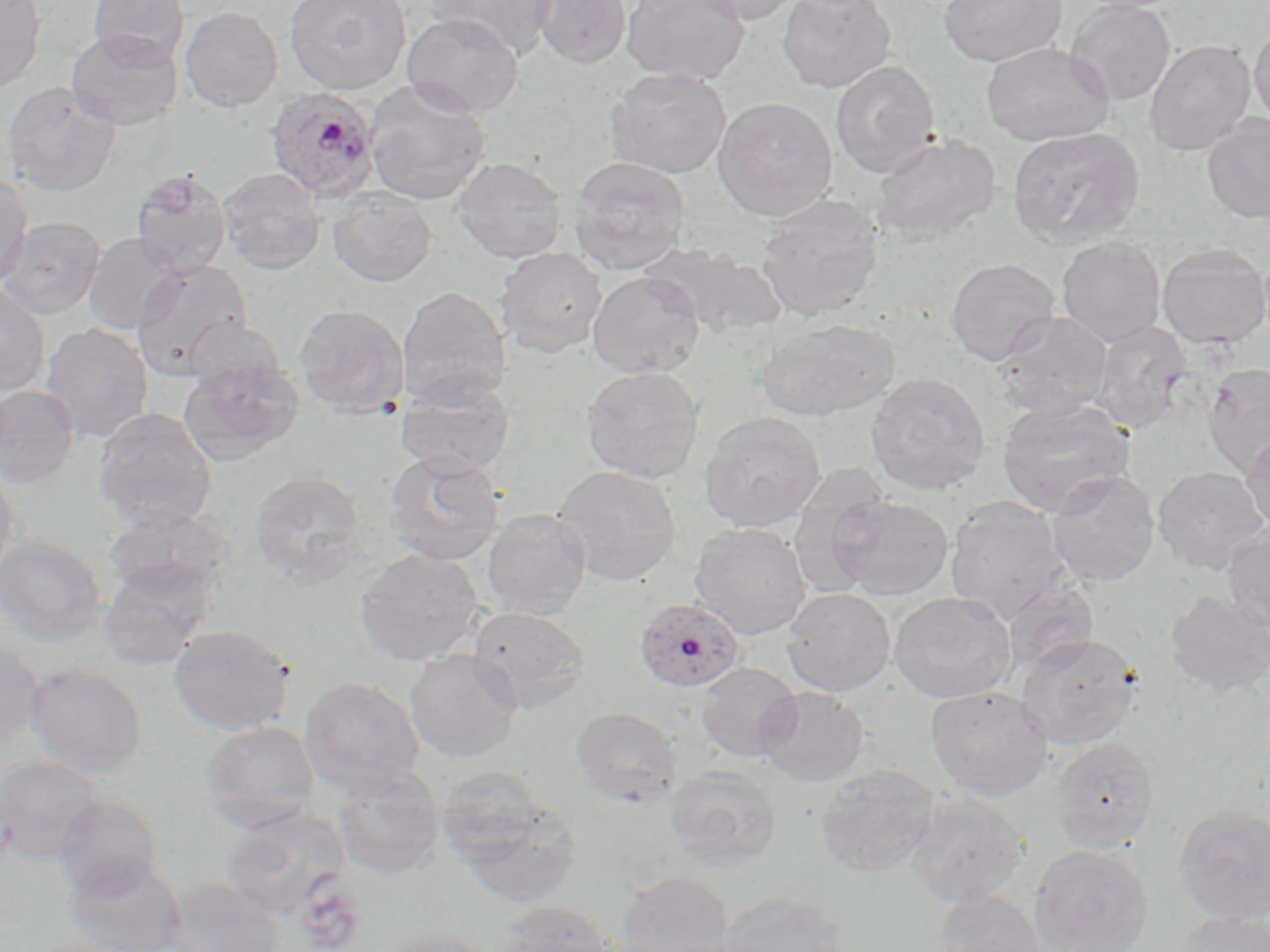 Approximate bounding boxes as (x1,y1)-(x2,y2) corner pairs in pixels. Plasmodium ovale-infected red blood cell locations: (264,86)-(382,204), (633,597)-(745,693). Uninfected red blood cell locations: (0,0)-(47,94), (87,0)-(190,67), (284,0)-(411,95), (424,0)-(557,57), (531,0)-(631,68), (621,0)-(751,85), (687,0)-(807,25), (777,0)-(897,93), (938,0)-(1067,67), (1065,0)-(1176,106), (178,5)-(404,107), (180,6)-(283,112), (402,13)-(524,117), (1249,23)-(1270,129), (65,29)-(183,130), (1145,39)-(1256,156), (981,43)-(1114,147), (830,59)-(940,178), (606,67)-(731,179), (364,80)-(491,206), (1,81)-(121,197), (712,97)-(837,221), (1201,113)-(1270,224), (1006,126)-(1145,249), (872,132)-(1001,244), (453,156)-(567,263), (569,156)-(690,274), (130,168)-(231,276), (219,168)-(326,275), (0,171)-(33,288), (328,187)-(436,287), (755,195)-(884,322), (0,216)-(106,319), (83,232)-(185,335), (1057,236)-(1166,347), (645,242)-(788,338), (1156,244)-(1269,349), (496,247)-(607,357), (945,257)-(1061,366), (131,259)-(254,380), (587,270)-(706,379), (0,282)-(51,397), (398,286)-(511,407), (294,304)-(409,416), (994,311)-(1112,419), (757,319)-(897,421), (1089,320)-(1192,433), (40,323)-(153,442), (180,358)-(303,466), (1202,363)-(1270,478), (581,366)-(706,483), (866,373)-(990,494), (395,375)-(516,477), (0,385)-(80,488), (997,397)-(1136,517), (92,409)-(218,530), (699,411)-(826,532), (1241,429)-(1270,537), (384,451)-(507,565), (0,460)-(20,582), (553,465)-(682,586), (1151,466)-(1269,574), (1046,469)-(1160,586), (249,470)-(366,587), (787,476)-(891,601), (829,495)-(954,600), (945,496)-(1070,624), (103,506)-(236,603), (481,509)-(591,620), (689,522)-(812,639), (1222,526)-(1270,633), (0,532)-(106,645), (355,547)-(485,665), (98,559)-(215,670), (1001,580)-(1098,674), (782,587)-(895,696), (889,590)-(1017,703), (1164,591)-(1270,697), (467,606)-(591,713), (169,624)-(294,734), (1016,632)-(1144,750), (0,638)-(44,753), (405,649)-(523,762), (26,661)-(147,778), (695,662)-(802,761), (300,676)-(425,795), (755,685)-(869,786), (926,685)-(1054,800), (571,706)-(681,805), (200,721)-(321,826), (1049,736)-(1160,851), (0,754)-(108,864), (665,763)-(782,870), (814,765)-(940,879), (331,766)-(445,880), (443,783)-(581,908), (903,791)-(1031,906), (53,794)-(162,897), (1174,804)-(1270,924), (222,809)-(350,918), (1031,844)-(1153,952), (62,854)-(188,952), (614,870)-(733,951), (166,877)-(284,952), (935,889)-(1046,952), (717,890)-(851,952), (496,901)-(618,952), (1173,912)-(1269,952), (373,929)-(504,952). Slide-level diagnosis: Plasmodium ovale. Image is 1270×952 pixels. 1000x magnification. Light microscopy. Single field of view. May-Grünwald-Giemsa stain. Thin blood film.